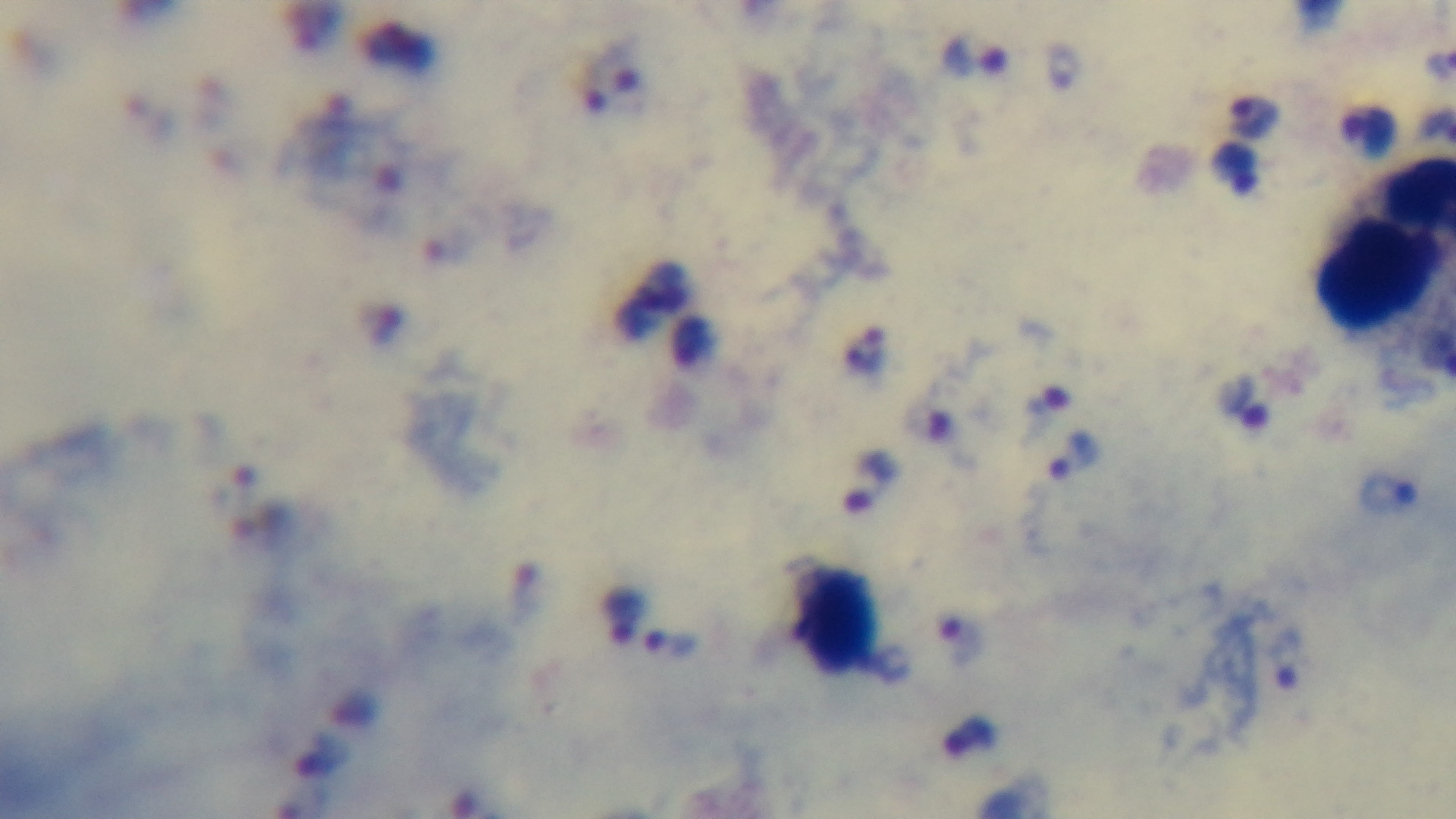
Summary:
  - Stain: Giemsa
  - Objective: 100x oil immersion
  - Field of view: single
  - Modality: light microscopy
  - Malaria status: infected
  - Capture: mounted 4K digital camera
  - Preparation: thick blood film